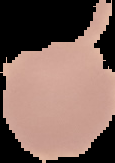
preparation = thin blood film
image size = 115×163 pixels
image type = cell region segmented out of the field of view; surrounding area masked to black
malaria status = uninfected